Classify this cell by malaria status.
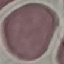
Uninfected.

{
  "capture": "smartphone camera at the microscope eyepiece",
  "stain": "Giemsa",
  "preparation": "thin smear",
  "image_type": "cell patch, automatically extracted from a larger field of view and resized to 64 × 64 pixels"
}